Identify the blood parasite species.
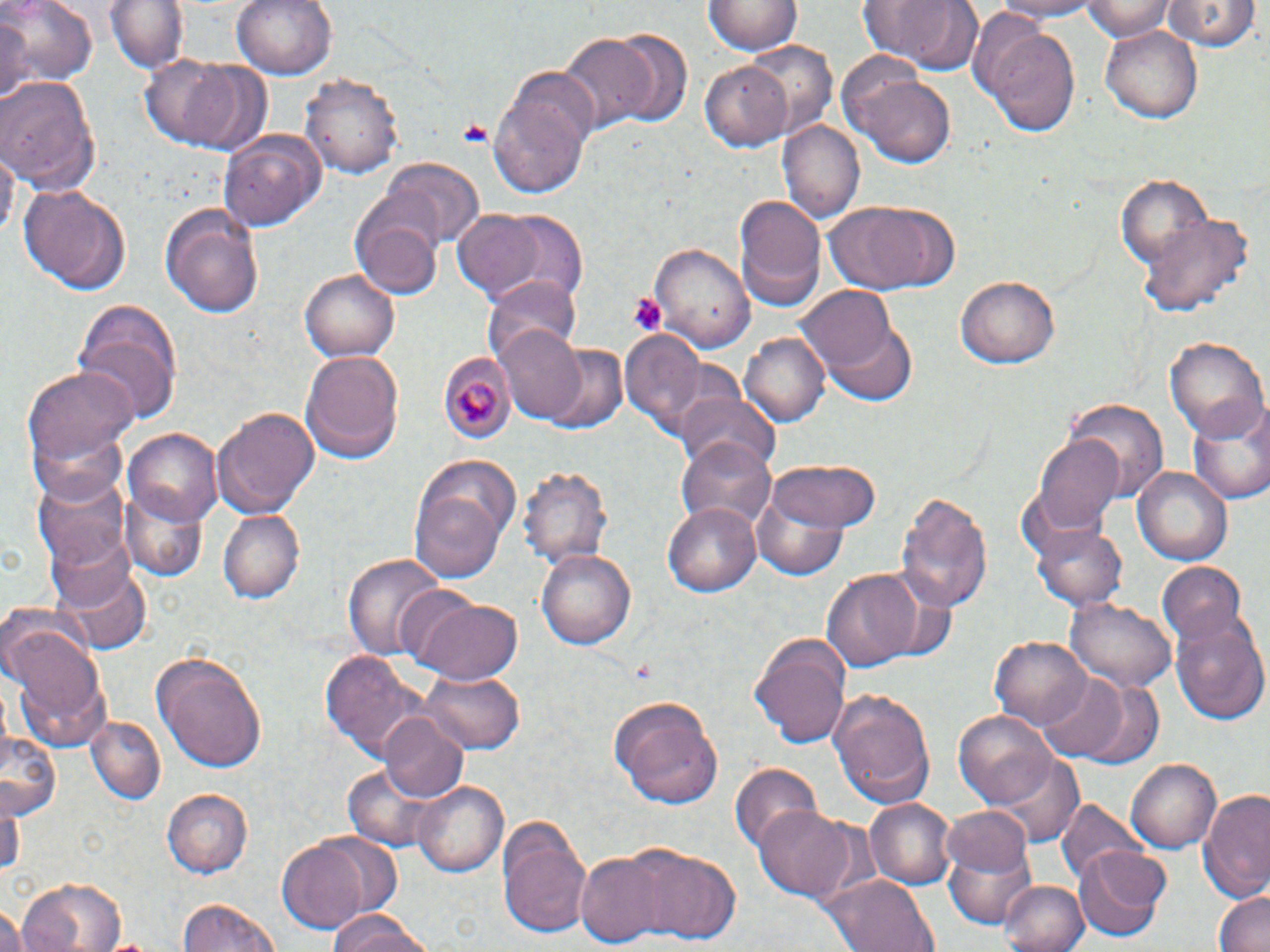
Plasmodium malariae.

uninfected red blood cell locations = approximate bounding boxes as named x1/y1/x2/y2 corners in pixels: (x1=2, y1=0, x2=96, y2=86), (x1=107, y1=0, x2=186, y2=76), (x1=231, y1=0, x2=338, y2=81), (x1=855, y1=0, x2=984, y2=72), (x1=988, y1=0, x2=1104, y2=20), (x1=1083, y1=0, x2=1176, y2=38), (x1=705, y1=1, x2=800, y2=56), (x1=1163, y1=2, x2=1256, y2=52), (x1=0, y1=8, x2=28, y2=112), (x1=975, y1=15, x2=1081, y2=137), (x1=1099, y1=25, x2=1203, y2=125), (x1=601, y1=30, x2=690, y2=126), (x1=558, y1=32, x2=658, y2=132), (x1=741, y1=40, x2=837, y2=136), (x1=143, y1=55, x2=267, y2=153), (x1=701, y1=60, x2=795, y2=149), (x1=490, y1=65, x2=599, y2=198), (x1=855, y1=69, x2=959, y2=166), (x1=301, y1=70, x2=405, y2=180), (x1=0, y1=74, x2=102, y2=194), (x1=779, y1=119, x2=864, y2=226), (x1=219, y1=130, x2=326, y2=230), (x1=384, y1=160, x2=484, y2=250), (x1=1116, y1=171, x2=1217, y2=278), (x1=17, y1=182, x2=133, y2=294), (x1=351, y1=193, x2=447, y2=297), (x1=732, y1=195, x2=827, y2=309), (x1=824, y1=199, x2=958, y2=295), (x1=161, y1=201, x2=266, y2=318), (x1=452, y1=209, x2=547, y2=299), (x1=485, y1=209, x2=589, y2=301), (x1=1141, y1=213, x2=1252, y2=318), (x1=652, y1=241, x2=754, y2=355), (x1=298, y1=266, x2=402, y2=362), (x1=483, y1=273, x2=583, y2=368), (x1=957, y1=275, x2=1060, y2=369), (x1=801, y1=285, x2=902, y2=381), (x1=72, y1=299, x2=184, y2=421), (x1=818, y1=310, x2=918, y2=404), (x1=494, y1=326, x2=590, y2=423), (x1=619, y1=327, x2=709, y2=434), (x1=740, y1=331, x2=829, y2=428), (x1=1163, y1=334, x2=1267, y2=442), (x1=538, y1=343, x2=628, y2=435), (x1=299, y1=349, x2=404, y2=465), (x1=19, y1=366, x2=138, y2=486), (x1=674, y1=391, x2=782, y2=471), (x1=1064, y1=398, x2=1167, y2=498), (x1=1190, y1=399, x2=1270, y2=505), (x1=212, y1=406, x2=319, y2=519), (x1=126, y1=428, x2=221, y2=523), (x1=1033, y1=433, x2=1125, y2=537), (x1=677, y1=435, x2=780, y2=536), (x1=409, y1=458, x2=520, y2=583), (x1=766, y1=459, x2=884, y2=533), (x1=518, y1=466, x2=612, y2=570), (x1=1132, y1=466, x2=1231, y2=567), (x1=33, y1=468, x2=132, y2=571), (x1=752, y1=485, x2=851, y2=583), (x1=121, y1=487, x2=208, y2=580), (x1=896, y1=490, x2=993, y2=611), (x1=664, y1=500, x2=763, y2=598), (x1=218, y1=507, x2=303, y2=601), (x1=1032, y1=518, x2=1131, y2=610), (x1=537, y1=547, x2=636, y2=650), (x1=344, y1=552, x2=447, y2=659), (x1=1156, y1=561, x2=1248, y2=652), (x1=56, y1=565, x2=149, y2=655), (x1=818, y1=568, x2=922, y2=672), (x1=411, y1=596, x2=523, y2=685), (x1=1066, y1=596, x2=1176, y2=692), (x1=1169, y1=609, x2=1269, y2=725), (x1=5, y1=625, x2=109, y2=749), (x1=990, y1=632, x2=1092, y2=729), (x1=750, y1=634, x2=851, y2=753), (x1=319, y1=649, x2=433, y2=761), (x1=154, y1=651, x2=267, y2=771), (x1=417, y1=670, x2=523, y2=753), (x1=1037, y1=674, x2=1129, y2=761), (x1=1069, y1=677, x2=1165, y2=771), (x1=826, y1=687, x2=935, y2=809), (x1=608, y1=696, x2=724, y2=809), (x1=955, y1=710, x2=1057, y2=807), (x1=378, y1=712, x2=469, y2=802), (x1=87, y1=714, x2=165, y2=803), (x1=2, y1=727, x2=61, y2=818), (x1=992, y1=753, x2=1085, y2=849), (x1=1124, y1=756, x2=1224, y2=855), (x1=729, y1=762, x2=823, y2=857), (x1=413, y1=781, x2=509, y2=877), (x1=1, y1=788, x2=24, y2=884), (x1=164, y1=788, x2=252, y2=878), (x1=1197, y1=788, x2=1270, y2=901), (x1=865, y1=798, x2=955, y2=890), (x1=1058, y1=799, x2=1149, y2=889), (x1=752, y1=805, x2=856, y2=900), (x1=942, y1=806, x2=1034, y2=879), (x1=496, y1=813, x2=594, y2=939), (x1=940, y1=835, x2=1040, y2=930), (x1=275, y1=838, x2=375, y2=934), (x1=628, y1=846, x2=741, y2=944), (x1=1073, y1=848, x2=1169, y2=941), (x1=575, y1=852, x2=670, y2=946), (x1=823, y1=873, x2=937, y2=952), (x1=17, y1=876, x2=125, y2=952), (x1=998, y1=878, x2=1088, y2=952), (x1=1212, y1=888, x2=1270, y2=952), (x1=177, y1=897, x2=282, y2=952), (x1=1, y1=908, x2=26, y2=952), (x1=325, y1=911, x2=439, y2=952)
Plasmodium malariae-infected red blood cell locations = approximate bounding boxes as named x1/y1/x2/y2 corners in pixels: (x1=440, y1=351, x2=515, y2=445)
field of view = single
preparation = thin blood film
magnification = 1000x
modality = light microscopy
image size = 1270×952 pixels
stain = May-Grünwald-Giemsa
platelet locations = approximate bounding boxes as named x1/y1/x2/y2 corners in pixels: (x1=455, y1=119, x2=495, y2=146), (x1=628, y1=292, x2=667, y2=334)